Locate every blood parasite and identify its species.
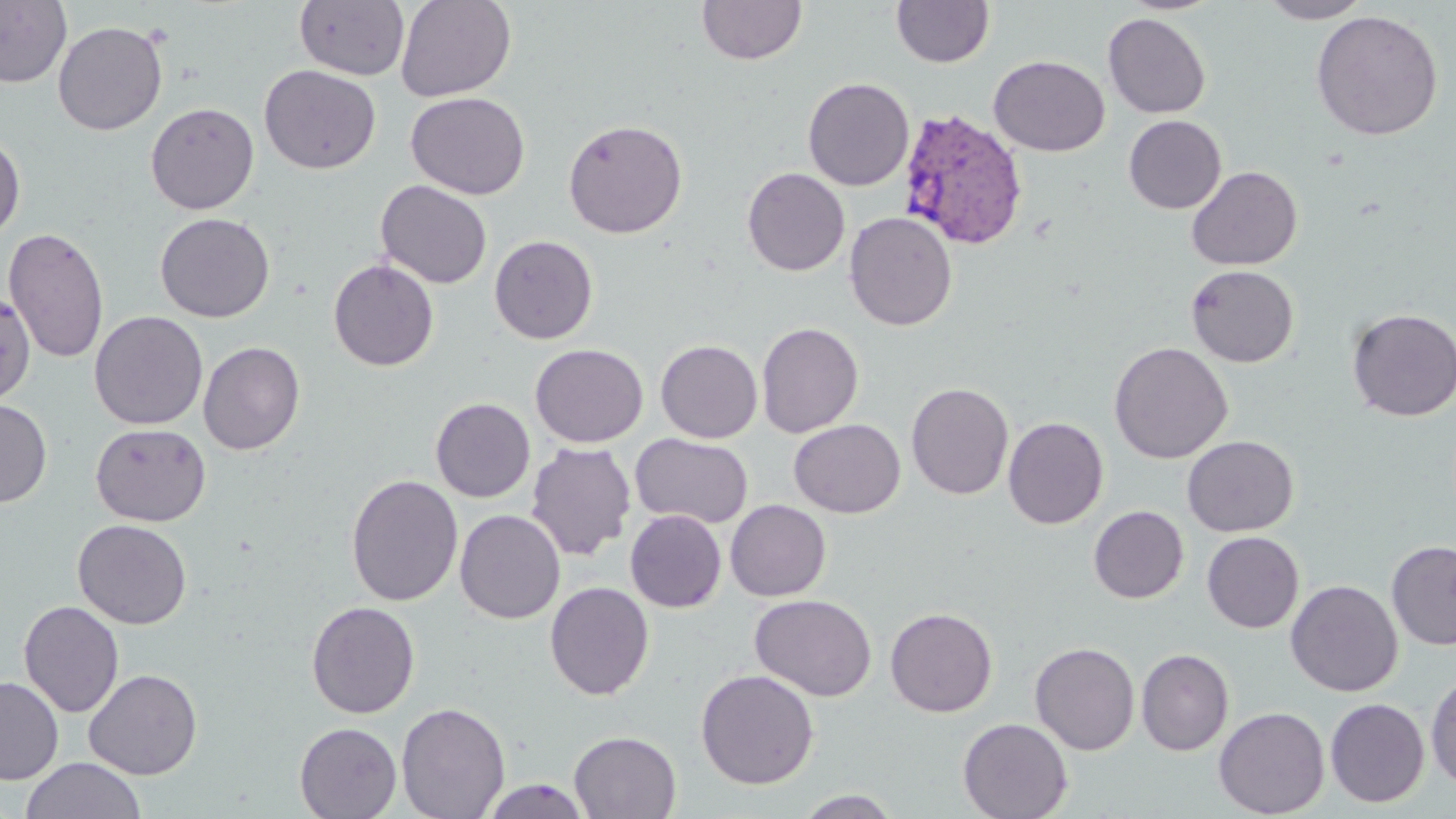

Approximate bounding boxes as (x1, y1, x2, y2) in pixels.
Plasmodium vivax-infected red blood cells: (898, 109, 1029, 250).
No Plasmodium falciparum, Plasmodium ovale, Plasmodium malariae, Babesia divergens, or Trypanosoma brucei observed.

Uninfected red blood cell locations: (395, 0, 517, 102), (891, 0, 994, 68), (1259, 0, 1373, 23), (0, 1, 71, 89), (294, 1, 409, 81), (697, 1, 807, 66), (1311, 9, 1443, 140), (1102, 12, 1211, 119), (52, 20, 168, 136), (989, 55, 1110, 156), (259, 64, 380, 174), (803, 77, 914, 191), (406, 92, 531, 199), (145, 102, 260, 214), (1123, 115, 1226, 214), (562, 118, 688, 239), (0, 133, 25, 242), (1186, 166, 1302, 271), (742, 167, 850, 276), (376, 180, 492, 288), (844, 211, 957, 331), (155, 213, 274, 322), (3, 227, 109, 364), (489, 235, 598, 344), (328, 258, 439, 371), (1185, 264, 1299, 367), (0, 293, 28, 407), (1346, 307, 1456, 421), (89, 310, 208, 430), (756, 321, 864, 437), (655, 339, 763, 443), (198, 341, 305, 455), (1108, 341, 1233, 464), (530, 343, 648, 448), (906, 382, 1014, 500), (430, 397, 536, 502), (0, 398, 53, 508), (1003, 416, 1108, 529), (789, 419, 905, 518), (90, 423, 211, 526), (630, 433, 754, 529), (1182, 435, 1299, 537), (525, 441, 637, 561), (345, 474, 463, 607), (725, 499, 831, 601), (1088, 505, 1188, 603), (454, 509, 565, 624), (625, 509, 727, 612), (72, 519, 191, 629), (1202, 531, 1304, 633), (1386, 540, 1456, 650), (1285, 579, 1403, 697), (544, 581, 654, 701), (749, 594, 878, 702), (19, 600, 124, 718), (305, 600, 420, 718), (885, 607, 998, 717), (1029, 641, 1140, 755), (1136, 648, 1234, 756), (695, 668, 819, 789), (84, 669, 202, 780), (1425, 672, 1456, 790), (0, 677, 64, 785), (1325, 698, 1430, 807), (396, 701, 510, 819), (1213, 707, 1330, 817), (957, 717, 1073, 819), (294, 722, 402, 819), (569, 730, 681, 818), (21, 757, 147, 819), (481, 778, 593, 818), (795, 789, 903, 818). Slide-level diagnosis: Plasmodium vivax. May-Grünwald-Giemsa stain. Image is 1456×819 pixels. 1000x magnification. One field of a larger specimen. Optical microscopy. Thin blood smear.